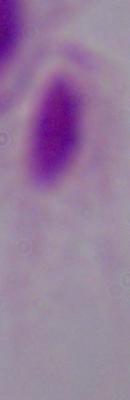
Summary:
  - Modality: micrograph
  - Identification: trichomonad
  - Magnification: 1000x